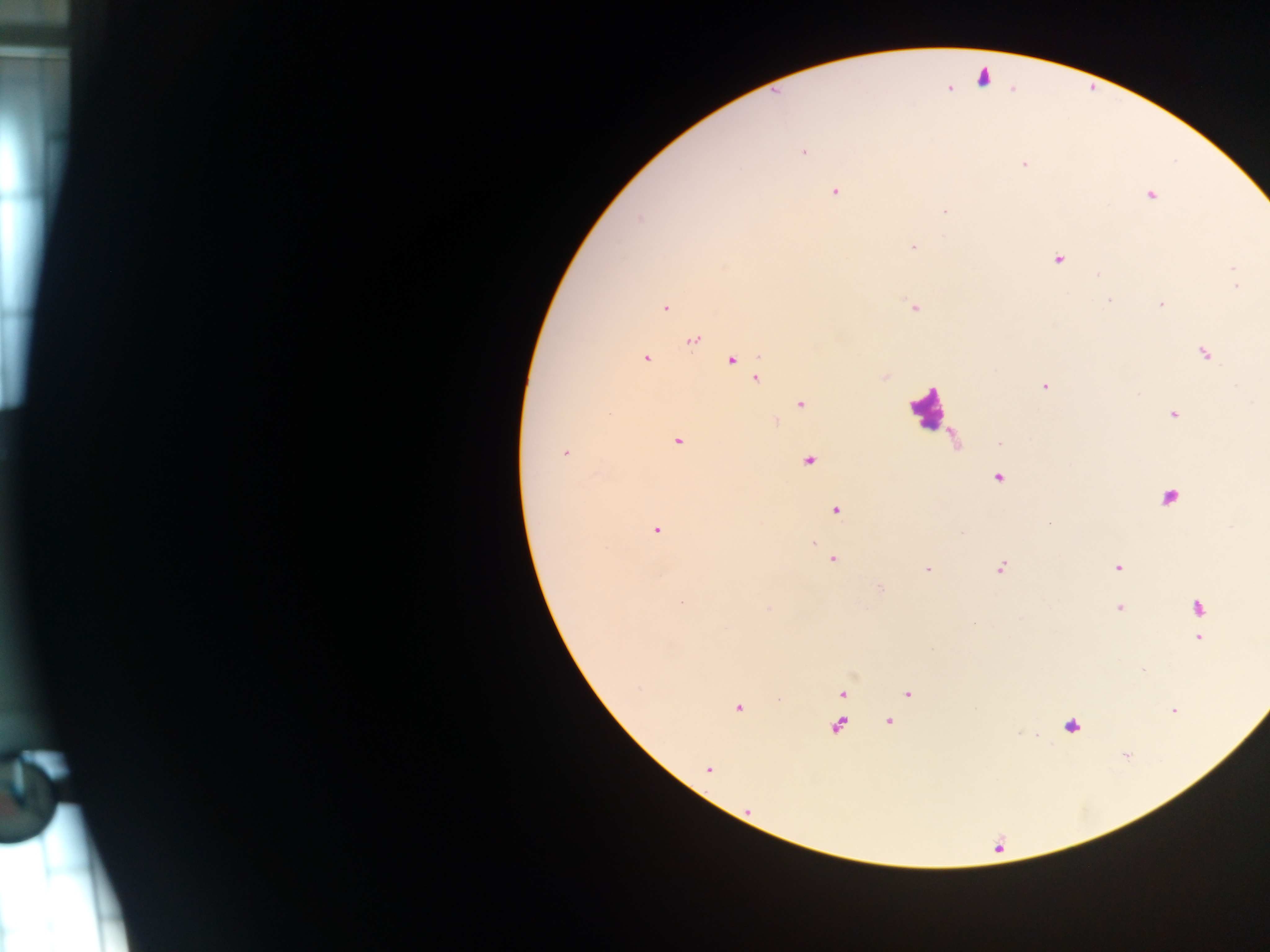

Approximate centers as (x, y) in pixels.
Summary:
  - Malaria parasite locations: (983, 77), (950, 88), (803, 151), (1023, 165), (835, 191), (1151, 195), (944, 211), (914, 246), (1059, 259), (1233, 268), (1237, 286), (1110, 301), (1161, 304), (915, 307), (665, 308), (693, 340), (1204, 353), (646, 358), (732, 360), (885, 377), (757, 379), (1044, 385), (801, 404), (1174, 414), (678, 441), (565, 452), (809, 460), (999, 477), (836, 510), (657, 529), (813, 542), (832, 560), (1001, 567), (1117, 567), (928, 569), (881, 587), (681, 603), (1120, 608), (1198, 608), (974, 624), (1198, 638), (1143, 670), (842, 693), (908, 694), (738, 708), (1173, 710), (888, 722), (1071, 725), (838, 726), (1125, 755), (709, 769)
  - Leukocyte locations: (926, 408)
  - Country: Ghana
  - Capture: mobile-phone photograph through a microscope
  - Field of view: single
  - Image size: 1270×952 pixels
  - Preparation: thick blood smear